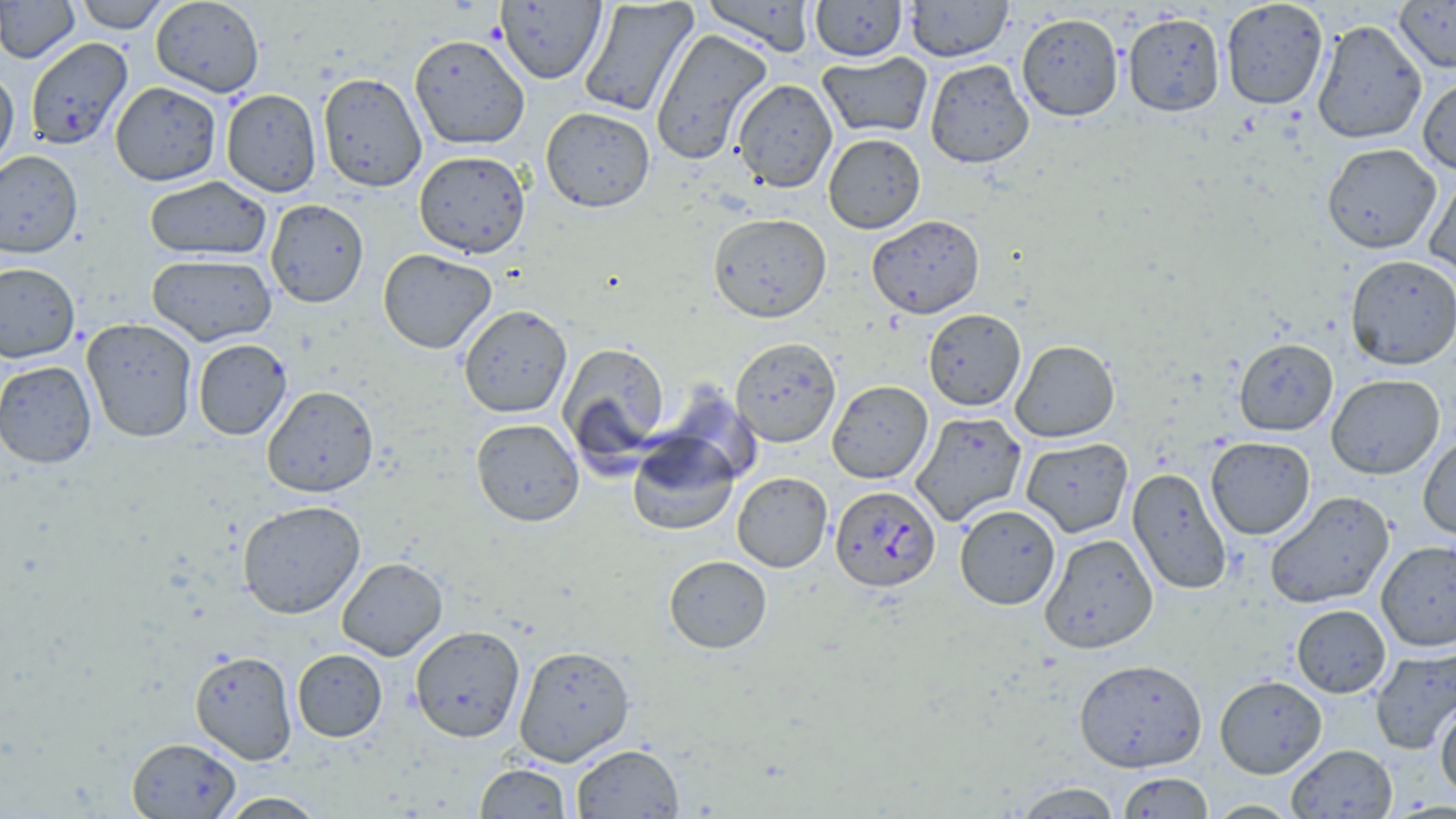

Approximate bounding boxes as (x1,y1)-(x2,y2) corner pairs in pixels. Plasmodium falciparum-infected red blood cell locations: (830,485)-(941,592). Uninfected red blood cell locations: (0,0)-(79,63), (74,0)-(171,33), (150,0)-(264,97), (495,0)-(606,84), (700,0)-(817,55), (808,0)-(908,62), (905,0)-(1013,62), (1220,0)-(1328,110), (578,1)-(698,117), (1395,1)-(1456,72), (1123,12)-(1225,117), (1016,13)-(1124,121), (1312,18)-(1427,144), (650,29)-(773,165), (408,33)-(529,150), (24,37)-(133,150), (817,52)-(932,139), (925,59)-(1034,168), (0,67)-(19,174), (318,72)-(427,192), (1417,76)-(1456,176), (733,79)-(837,192), (110,81)-(222,186), (220,89)-(322,197), (540,106)-(655,212), (823,133)-(925,234), (1322,143)-(1441,253), (0,150)-(83,258), (414,150)-(531,258), (1424,172)-(1456,284), (143,176)-(271,261), (265,199)-(368,308), (708,213)-(831,322), (867,214)-(985,318), (378,249)-(497,353), (147,253)-(277,345), (1344,254)-(1456,370), (0,262)-(80,363), (458,304)-(572,418), (923,308)-(1026,411), (82,318)-(197,443), (730,337)-(841,447), (1234,337)-(1338,436), (192,338)-(291,440), (1010,339)-(1120,442), (557,342)-(670,460), (0,360)-(97,469), (1326,374)-(1445,479), (827,380)-(933,483), (658,384)-(764,488), (262,385)-(379,497), (910,411)-(1028,526), (471,417)-(584,527), (627,433)-(739,535), (1418,433)-(1456,540), (1205,436)-(1315,540), (1021,437)-(1133,537), (1127,467)-(1233,595), (732,472)-(832,572), (1264,490)-(1395,609), (237,500)-(366,619), (955,504)-(1060,609), (1040,533)-(1159,653), (1375,540)-(1456,651), (664,554)-(772,653), (337,557)-(448,660), (1291,604)-(1391,697), (409,625)-(525,742), (514,644)-(635,766), (1370,647)-(1456,755), (292,649)-(387,741), (190,650)-(298,765), (1074,658)-(1207,772), (1215,675)-(1327,778), (1435,699)-(1456,800), (126,737)-(242,818), (571,743)-(684,818), (1287,743)-(1397,818), (475,763)-(572,818), (1117,772)-(1213,818), (1013,781)-(1123,818), (216,791)-(328,818), (1204,800)-(1301,818). Slide-level diagnosis: Plasmodium falciparum. Light microscopy. One field of a larger specimen. May-Grünwald-Giemsa stain. 1000x magnification. Image is 1456×819 pixels. Thin blood film.